Give the position of every malaria parasite and every leukocyte.
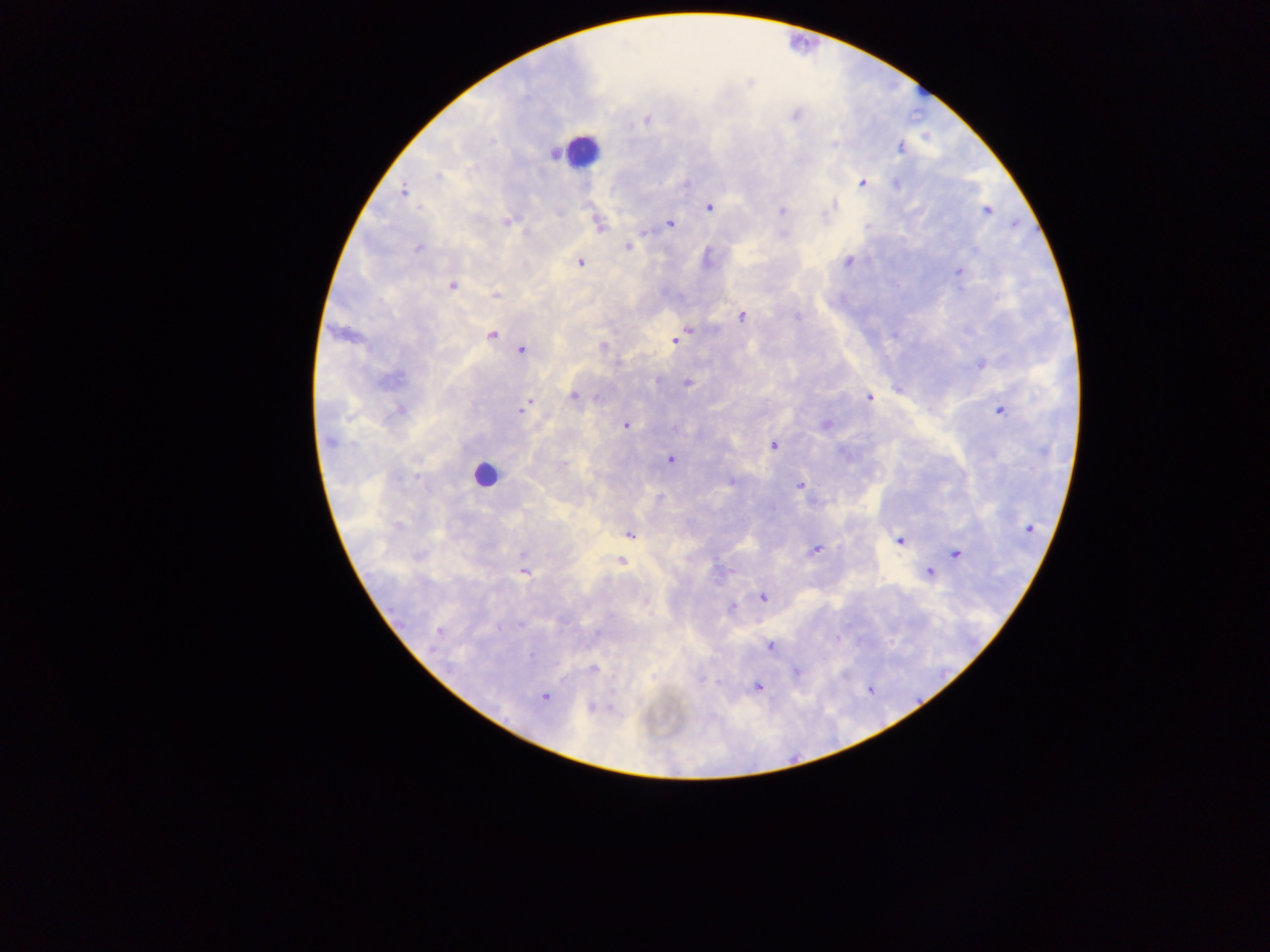
Approximate centers as (x, y) in pixels.
Malaria parasites: (795, 115), (647, 119), (900, 147), (439, 176), (687, 182), (862, 183), (897, 184), (403, 191), (835, 204), (709, 207), (781, 211), (987, 211), (506, 222), (670, 224), (598, 225), (418, 247), (628, 247), (848, 261), (581, 262), (958, 271), (451, 285), (495, 294), (742, 316), (797, 317), (687, 329), (492, 335), (675, 340), (522, 350), (980, 364), (399, 378), (687, 383), (573, 397), (598, 398), (870, 398), (524, 407), (400, 410), (999, 411), (625, 425), (827, 425), (676, 429), (330, 441), (774, 446), (669, 460), (732, 482), (800, 486), (772, 509), (1028, 529), (630, 534), (900, 541), (815, 549), (956, 553), (623, 556), (621, 561), (523, 573), (929, 573), (762, 596), (646, 602), (732, 607), (520, 625), (498, 628), (438, 632), (770, 646), (531, 656), (593, 668), (796, 671), (718, 683), (758, 687), (544, 697), (591, 707).
Leukocytes: (581, 151), (485, 474).

Summary:
  - Image size: 1270×952 pixels
  - Capture: mobile-phone photograph through a microscope
  - Field of view: single
  - Country: Ghana
  - Preparation: thick blood film